Classify this cell by malaria status.
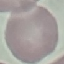
It is uninfected.

Summary:
  - Stain: Giemsa
  - Preparation: thin smear
  - Capture: smartphone through the microscope eyepiece
  - Image type: cell patch, automatically extracted from a larger field of view and resized to 64 × 64 pixels